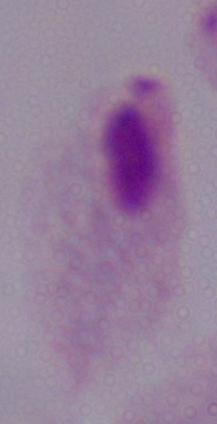

Summary:
  - Magnification: 1000x
  - Identification: trichomonad
  - Modality: micrograph